State which parasite is depicted.
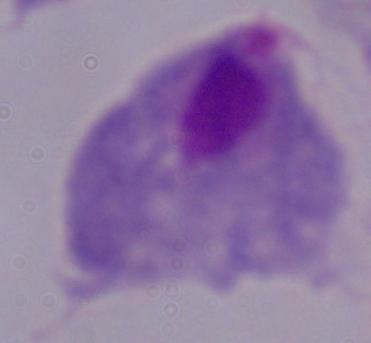
A trichomonad.

1000x magnification. Photomicrograph.